Report the malaria status.
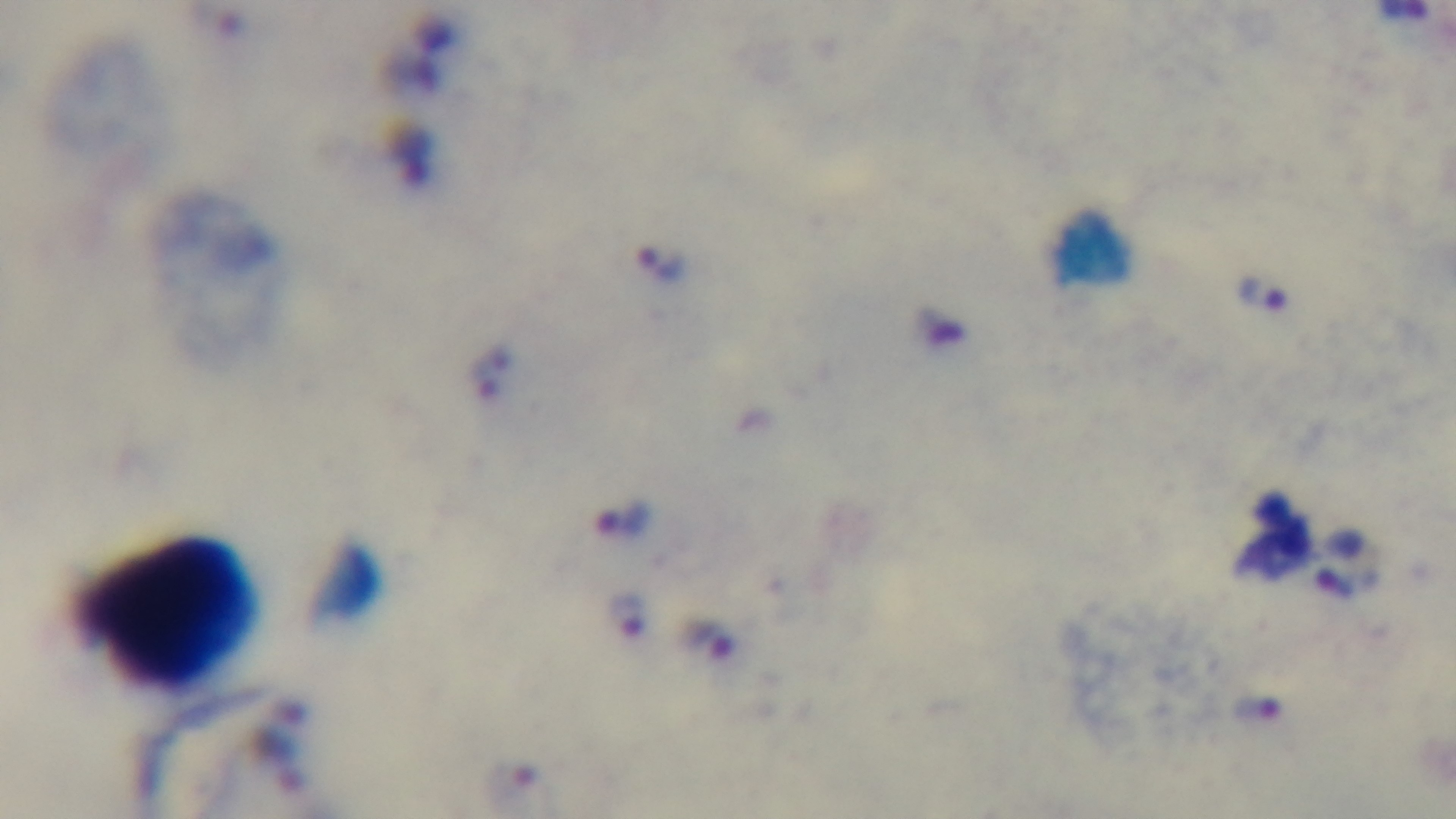
It is infected.

capture = mounted 4K digital camera
field of view = one from the slide
preparation = thick smear
stain = Giemsa
modality = light microscopy
objective = 100x oil immersion